Classify this cell by malaria status.
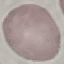

Uninfected.

stain = Giemsa
preparation = thin blood film
image type = cell patch, automatically extracted from a larger field of view and resized to 64 × 64 pixels
capture = smartphone camera at the microscope eyepiece